Classify this cell by malaria status.
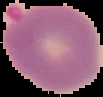

It is parasitized.

The area outside the segmented cell region is set to black. From a thin blood film. Image is 103×97 pixels.